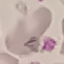
result: negative for malaria parasites
capture: smartphone camera at the microscope eyepiece
preparation: thin smear
image_type: automatically extracted cell patch, resized to 64 × 64 pixels
stain: Giemsa